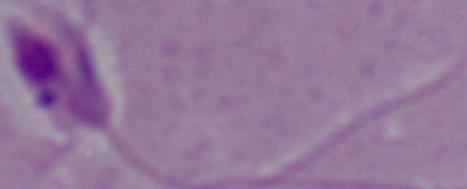

Summary:
  - Identification: Leishmania
  - Modality: micrograph
  - Magnification: 1000x